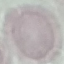

Malaria status: uninfected. Giemsa-stained preparation. Acquired by smartphone through the microscope eyepiece. Thin blood smear. Automatically extracted cell patch, resized to 64 × 64 pixels.